Name the parasite shown.
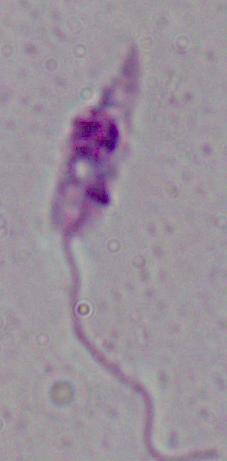

Leishmania.

{
  "modality": "micrograph",
  "magnification": "1000x"
}